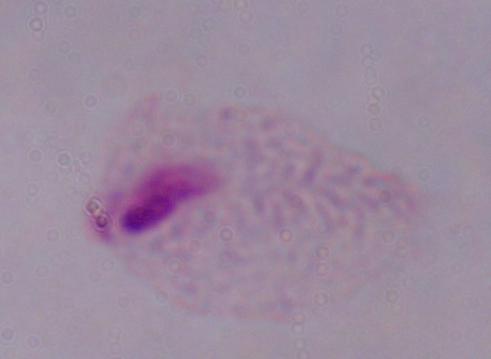
{
  "identification": "trichomonad",
  "modality": "micrograph",
  "magnification": "1000x"
}